Identify the parasite.
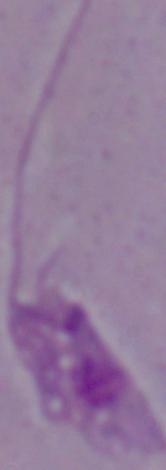

Leishmania.

Summary:
  - Modality: photomicrograph
  - Magnification: 1000x